Outline each uninfected red blood cell.
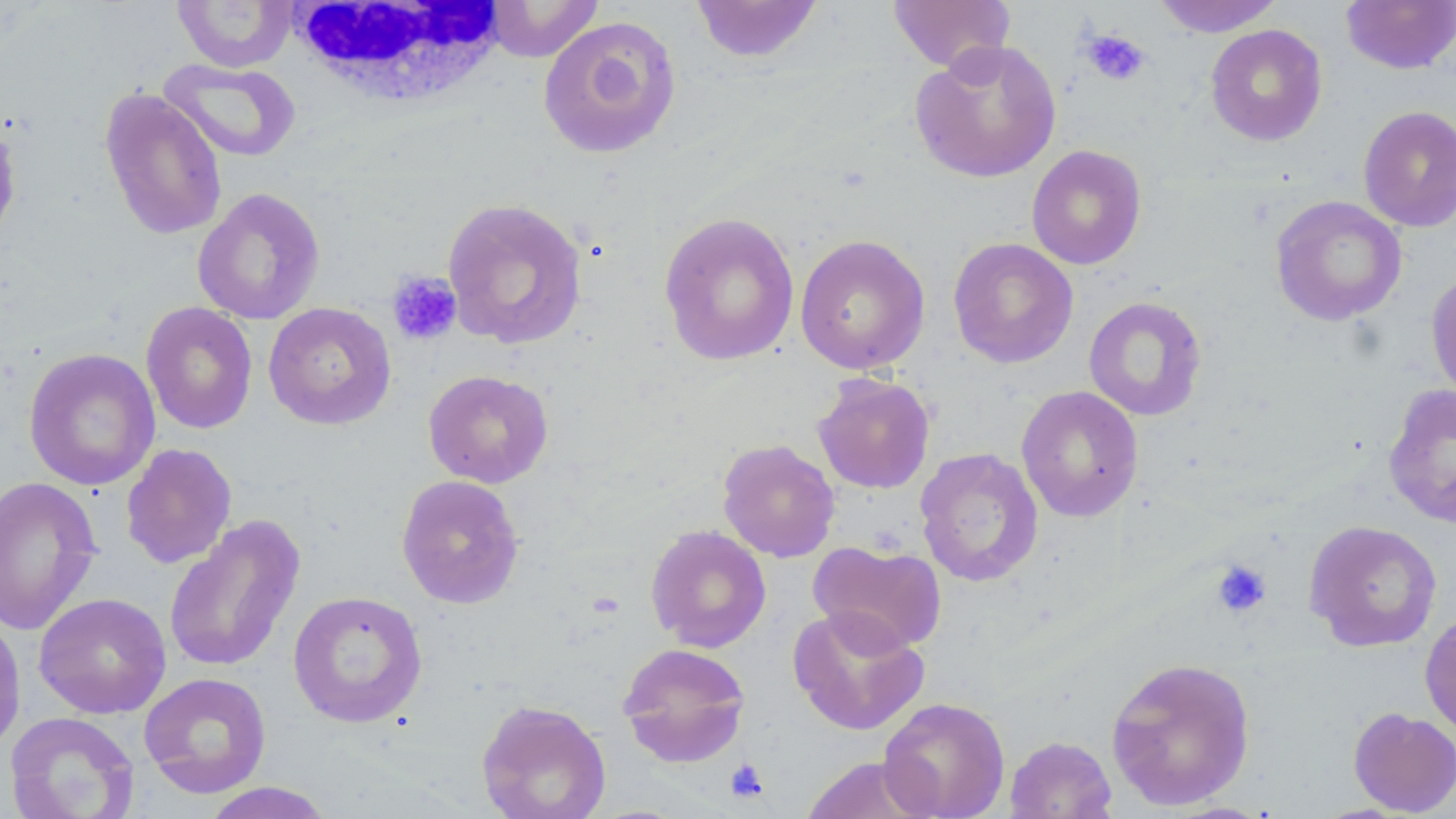
Approximate bounding boxes as [x1, y1, x2, y2] in pixels.
Uninfected red blood cells: [172, 0, 297, 71], [691, 0, 824, 64], [1152, 0, 1285, 37], [482, 1, 604, 62], [887, 1, 1016, 73], [1341, 1, 1456, 74], [537, 15, 682, 159], [1205, 24, 1328, 146], [909, 39, 1061, 183], [158, 58, 302, 163], [99, 88, 228, 241], [1358, 105, 1456, 232], [0, 113, 22, 252], [1027, 144, 1147, 270], [192, 187, 325, 326], [1270, 195, 1407, 326], [441, 196, 588, 350], [658, 211, 801, 367], [794, 233, 931, 374], [948, 237, 1078, 368], [1425, 270, 1456, 405], [1083, 296, 1207, 421], [140, 302, 258, 434], [263, 302, 396, 430], [23, 348, 161, 491], [423, 370, 554, 488], [812, 373, 935, 494], [1383, 384, 1456, 529], [1016, 385, 1144, 522], [716, 439, 840, 562], [120, 443, 237, 569], [915, 447, 1044, 587], [396, 474, 524, 609], [0, 476, 103, 636], [163, 514, 305, 675], [1303, 519, 1442, 652], [645, 524, 772, 652], [809, 540, 947, 655], [288, 590, 428, 728], [33, 592, 172, 718], [787, 605, 929, 735], [1420, 610, 1456, 740], [0, 613, 26, 757], [616, 642, 751, 768], [1105, 656, 1256, 810], [138, 672, 272, 798], [878, 697, 1011, 819], [476, 699, 612, 819], [1347, 707, 1456, 816], [4, 711, 140, 819], [1004, 735, 1117, 819], [799, 755, 933, 818], [199, 782, 336, 818].

White blood cell locations: [288, 0, 510, 109]. Platelet locations: [1081, 28, 1150, 86], [387, 271, 462, 346], [1210, 559, 1272, 619], [724, 757, 769, 804]. Slide-level diagnosis: negative for blood parasites. One field of a larger specimen. Captured at 1000x magnification. May-Grünwald-Giemsa stain. Light microscopy. Image is 1456×819 pixels. Thin blood film.